Locate every Plasmodium ovale-infected red blood cell.
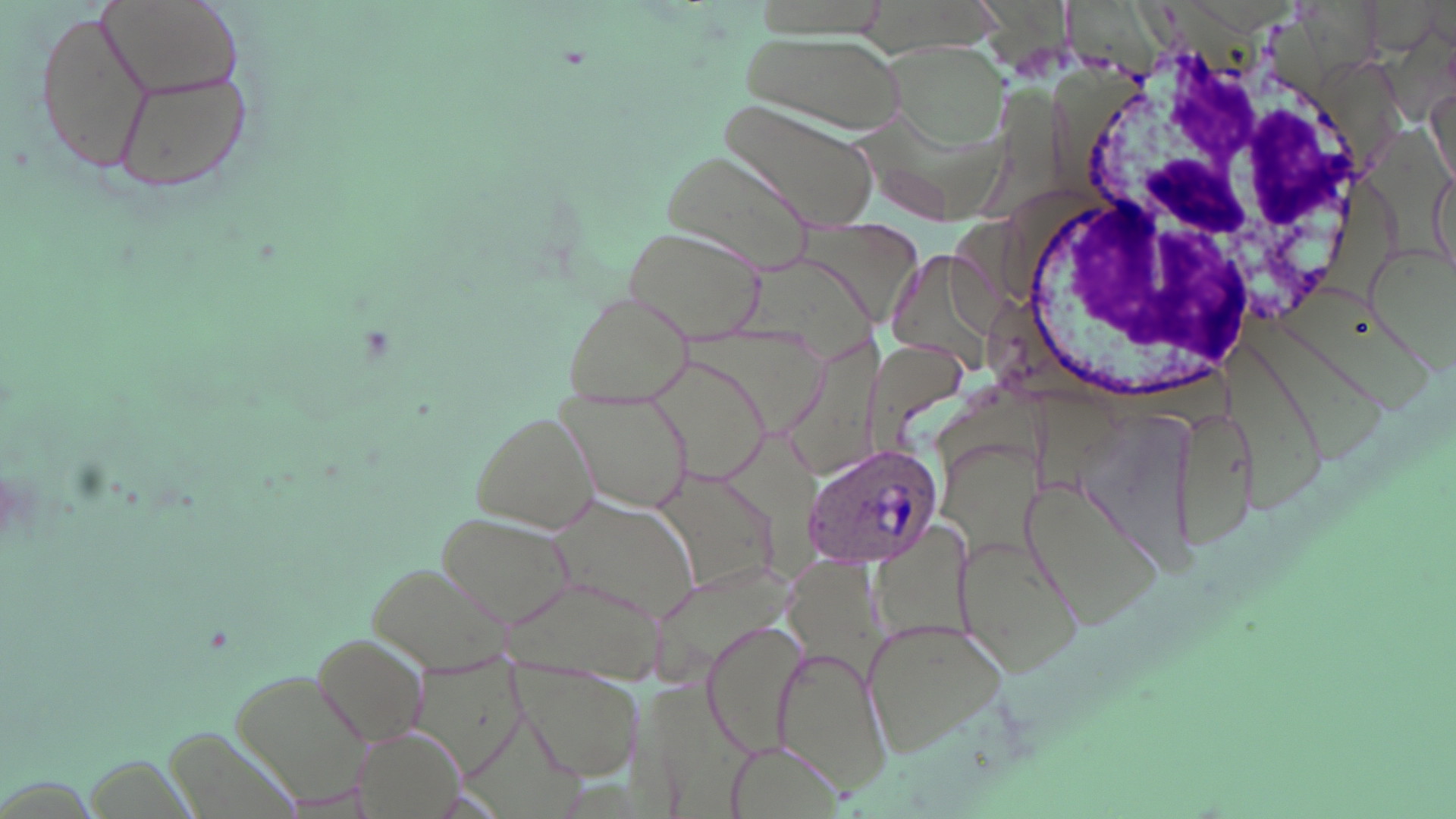
Approximate bounding boxes as [x1, y1, x2, y2] in pixels.
Plasmodium ovale-infected red blood cells: [800, 443, 944, 572].

slide-level diagnosis = Plasmodium ovale
white blood cell locations = approximate bounding boxes as [x1, y1, x2, y2] in pixels: [1015, 36, 1388, 407]
field of view = single
image size = 1456×819 pixels
modality = optical microscopy
stain = May-Grünwald-Giemsa
magnification = 1000x
uninfected red blood cell locations = approximate bounding boxes as [x1, y1, x2, y2] in pixels: [97, 0, 246, 101], [36, 4, 154, 175], [734, 30, 907, 136], [880, 39, 1009, 149], [107, 60, 255, 198], [1428, 84, 1453, 189], [717, 98, 878, 232], [662, 147, 818, 283], [1430, 163, 1452, 275], [623, 224, 764, 344], [562, 289, 696, 405], [643, 353, 775, 486], [563, 387, 696, 512], [1167, 397, 1259, 557], [467, 406, 602, 537], [648, 467, 785, 595], [1021, 479, 1161, 624], [548, 495, 703, 624], [434, 509, 576, 629], [955, 531, 1084, 676], [368, 557, 517, 675], [701, 617, 810, 759], [861, 617, 1009, 756], [312, 632, 431, 750], [773, 646, 893, 794], [507, 661, 642, 781], [227, 664, 378, 805], [723, 736, 842, 818]
preparation = thin blood film